Assess this cell for malaria.
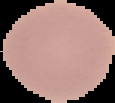

Uninfected.

image size = 115×103 pixels
image type = segmented cell region on a black background
preparation = thin blood smear